Locate every Plasmodium parasite.
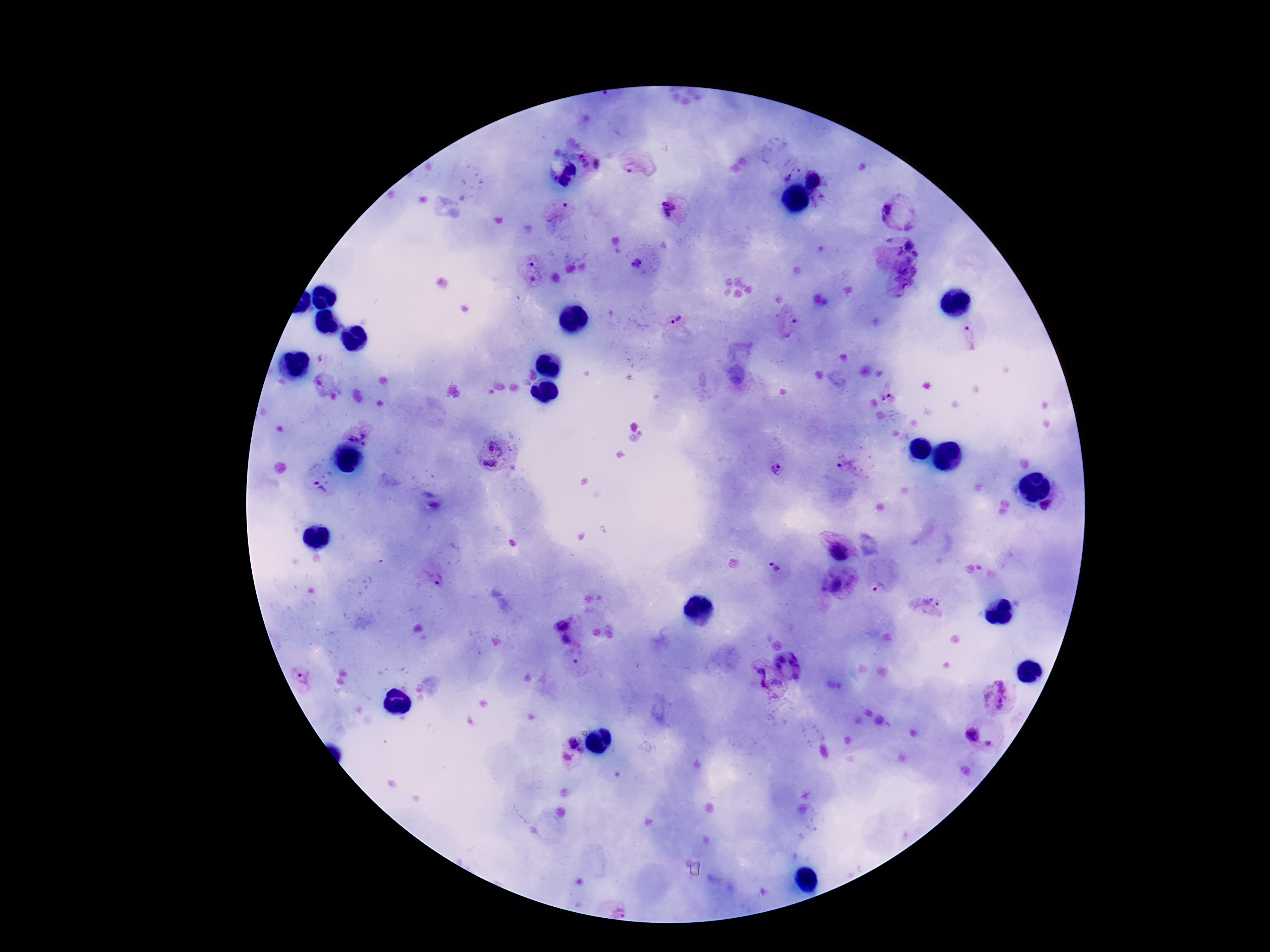
Approximate object centers, in pixels from the top-left corner.
Plasmodium parasites: (x=584, y=161), (x=638, y=163), (x=599, y=164), (x=788, y=175), (x=814, y=182), (x=565, y=207), (x=671, y=208), (x=890, y=213), (x=907, y=225), (x=908, y=244), (x=636, y=265), (x=533, y=270), (x=678, y=321), (x=794, y=328), (x=972, y=338), (x=887, y=397), (x=360, y=433), (x=495, y=457), (x=850, y=467), (x=775, y=469), (x=319, y=486), (x=838, y=551), (x=773, y=566), (x=435, y=580), (x=836, y=586), (x=877, y=589), (x=932, y=602), (x=562, y=622), (x=569, y=640), (x=797, y=657), (x=781, y=659), (x=778, y=667), (x=761, y=670), (x=302, y=677), (x=795, y=677), (x=778, y=683), (x=763, y=686), (x=998, y=694), (x=973, y=735), (x=573, y=745), (x=993, y=745), (x=567, y=758), (x=619, y=906).

Image is 1270×952 pixels. Photographed through the microscope eyepiece with a smartphone camera. Giemsa-stained preparation. Thick blood film. 100x magnification. One field from this slide. Patient malaria status: positive.